Assess this cell for malaria.
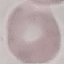

Uninfected.

Giemsa-stained preparation. Cell patch, automatically extracted from a larger field of view and resized to 64 × 64 pixels. Thin smear of blood. Acquired by smartphone through the microscope eyepiece.